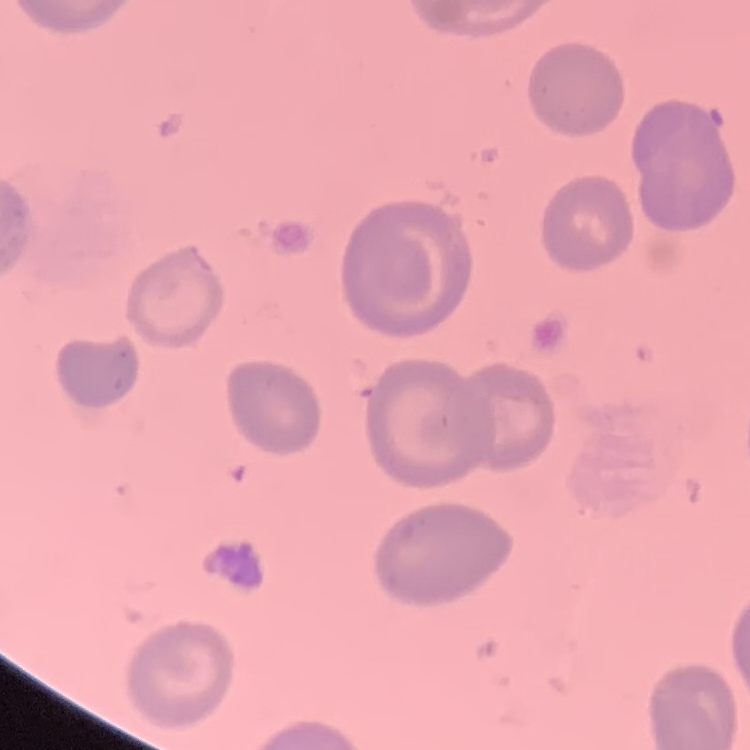
Summary:
  - Red blood cell morphology: no rouleaux formation
  - Preparation: thin blood film
  - Stain: Field's or Giemsa
  - Image type: one tile cut from a larger photomicrograph